Locate every Plasmodium parasite.
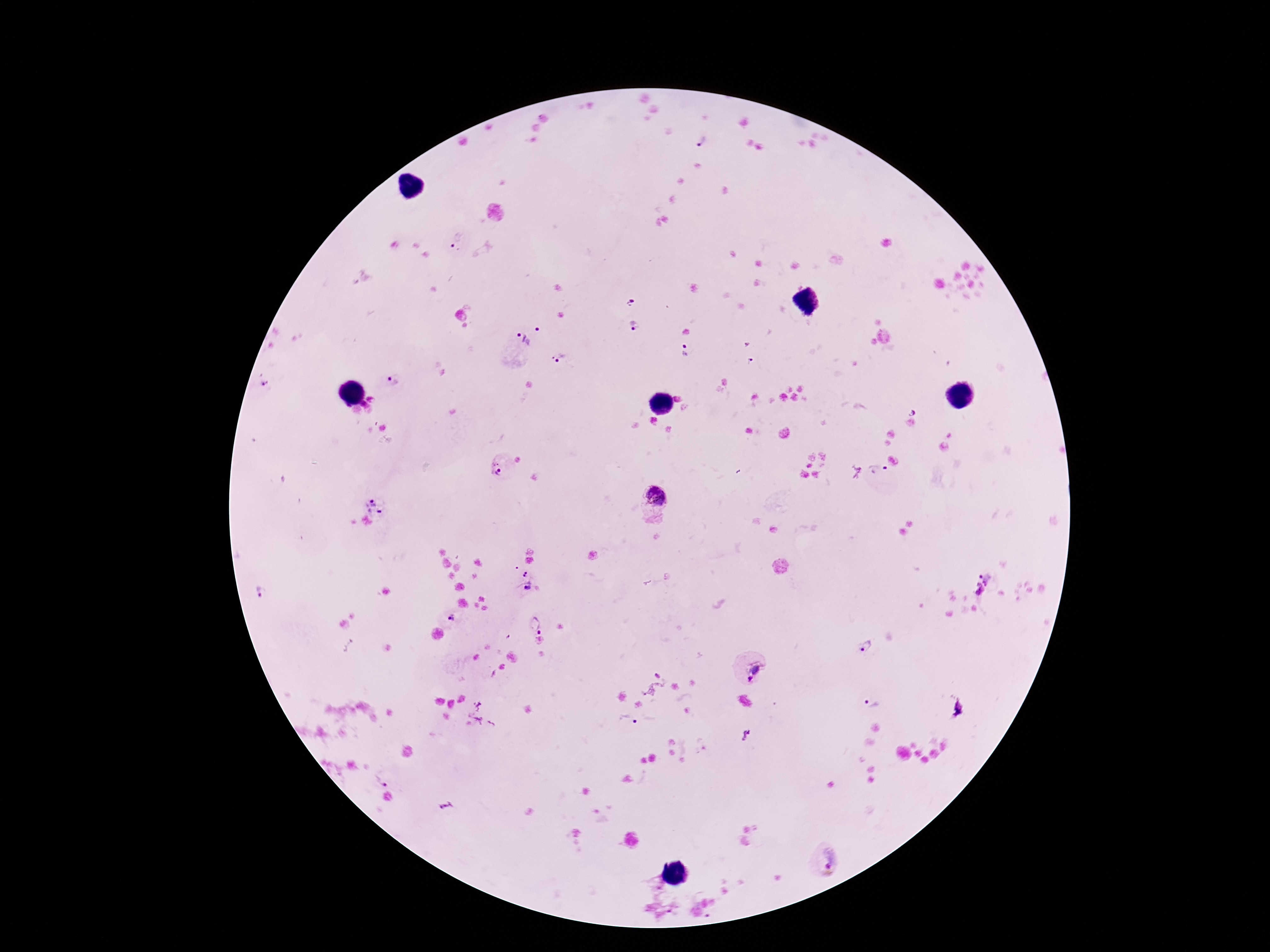

Approximate object centers, in pixels from the top-left corner.
Plasmodium parasites: (x=702, y=142), (x=455, y=241), (x=630, y=301), (x=635, y=326), (x=528, y=336), (x=747, y=345), (x=685, y=349), (x=562, y=358), (x=751, y=361), (x=392, y=382), (x=265, y=384), (x=372, y=398), (x=365, y=406), (x=913, y=412), (x=496, y=466), (x=877, y=470), (x=656, y=495), (x=376, y=502), (x=529, y=573), (x=981, y=583), (x=528, y=587), (x=263, y=592), (x=452, y=618), (x=535, y=624), (x=867, y=647), (x=757, y=668), (x=655, y=674), (x=750, y=678), (x=870, y=703), (x=629, y=721), (x=746, y=735), (x=383, y=778), (x=446, y=806), (x=824, y=861).

Patient malaria status: positive. One field from this slide. 100x magnification. Giemsa stain. Thick peripheral-blood smear. Image is 1270×952 pixels. Smartphone photograph taken through the microscope eyepiece.